Assess this cell for malaria.
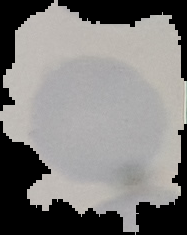
It is uninfected.

Summary:
  - Image size: 187×235 pixels
  - Preparation: thin blood film
  - Image type: segmented cell region on a black background